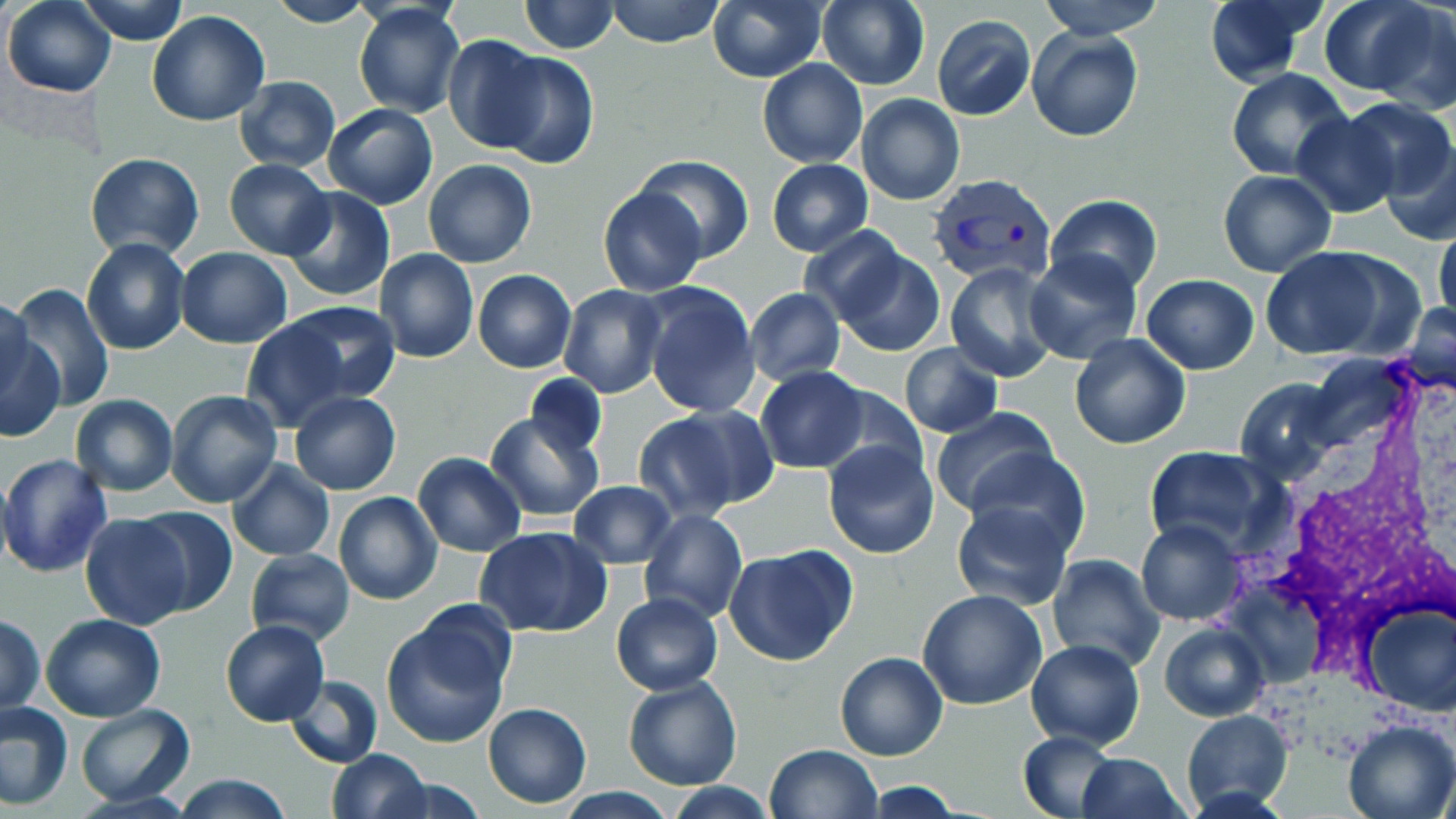
Plasmodium vivax-infected red blood cell locations = approximate bounding boxes as [x1, y1, x2, y2] in pixels: [927, 170, 1058, 286]
slide-level diagnosis = Plasmodium vivax
image size = 1456×819 pixels
modality = optical microscopy
preparation = thin blood film
magnification = 1000x
field of view = one of a larger specimen
uninfected red blood cell locations = approximate bounding boxes as [x1, y1, x2, y2] in pixels: [3, 0, 116, 97], [76, 0, 190, 44], [519, 0, 618, 53], [604, 0, 725, 47], [708, 0, 827, 83], [816, 0, 930, 89], [1040, 0, 1162, 40], [1202, 0, 1324, 87], [1318, 0, 1437, 96], [265, 1, 374, 28], [1370, 2, 1456, 116], [353, 3, 464, 117], [148, 11, 272, 127], [932, 15, 1035, 120], [1028, 29, 1143, 144], [442, 35, 550, 153], [490, 51, 599, 170], [757, 59, 867, 167], [1227, 68, 1351, 181], [235, 76, 341, 172], [855, 93, 965, 205], [1337, 98, 1454, 202], [323, 102, 438, 210], [1291, 112, 1401, 218], [1381, 140, 1456, 247], [85, 151, 204, 260], [635, 154, 754, 263], [224, 158, 334, 260], [767, 159, 873, 255], [424, 160, 536, 267], [1219, 170, 1337, 277], [281, 186, 395, 302], [598, 186, 707, 296], [1044, 195, 1162, 294], [1434, 221, 1456, 333], [798, 225, 910, 327], [81, 237, 190, 355], [831, 244, 945, 356], [174, 246, 292, 348], [1257, 248, 1400, 361], [375, 249, 480, 364], [1024, 251, 1142, 365], [944, 263, 1060, 382], [473, 269, 577, 374], [1141, 274, 1259, 373], [639, 281, 762, 418], [9, 284, 114, 412], [558, 285, 669, 400], [744, 287, 846, 385], [0, 295, 32, 408], [283, 301, 401, 406], [1400, 305, 1456, 392], [240, 318, 356, 433], [1, 322, 65, 444], [1069, 332, 1191, 449], [899, 343, 1001, 437], [754, 367, 868, 473], [525, 373, 606, 458], [1237, 377, 1338, 481], [823, 386, 929, 482], [166, 390, 283, 509], [289, 391, 402, 495], [70, 395, 179, 494], [633, 406, 770, 519], [930, 406, 1060, 519], [485, 411, 604, 522], [824, 440, 939, 558], [1143, 447, 1276, 554], [964, 448, 1090, 556], [412, 453, 526, 557], [0, 454, 113, 578], [227, 460, 335, 562], [569, 480, 677, 568], [333, 492, 443, 605], [951, 501, 1073, 610], [132, 504, 238, 616], [639, 509, 748, 625], [80, 512, 194, 630], [1135, 518, 1246, 626], [476, 528, 611, 638], [724, 543, 858, 667], [244, 549, 357, 646], [1046, 555, 1165, 672], [917, 589, 1047, 710], [610, 592, 723, 694], [1360, 602, 1455, 715], [380, 610, 515, 750], [1, 614, 45, 718], [41, 614, 166, 723], [220, 620, 329, 727], [1159, 621, 1270, 722], [1025, 639, 1144, 751], [835, 650, 948, 761], [284, 674, 383, 768], [623, 676, 742, 790], [0, 701, 74, 808], [482, 701, 592, 808], [75, 703, 195, 805], [1182, 709, 1294, 816], [1342, 718, 1456, 819], [1018, 731, 1120, 817], [764, 743, 883, 819], [326, 749, 430, 819], [1076, 752, 1189, 819], [171, 774, 294, 818], [384, 775, 486, 817], [864, 781, 963, 818], [664, 782, 779, 818], [554, 789, 677, 819]
stain = May-Grünwald-Giemsa
white blood cell locations = approximate bounding boxes as [x1, y1, x2, y2] in pixels: [1239, 363, 1456, 675]